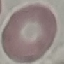

Summary:
  - Result: no malaria parasites detected
  - Capture: smartphone through the microscope eyepiece
  - Stain: Giemsa
  - Preparation: thin blood film
  - Image type: automatically extracted cell patch, resized to 64 × 64 pixels